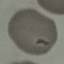
{
  "result": "no malaria parasites seen",
  "image_type": "automatically extracted cell patch, resized to 64 × 64 pixels",
  "capture": "smartphone camera at the microscope eyepiece",
  "stain": "Giemsa",
  "preparation": "thin smear"
}